Locate every Plasmodium malariae-infected red blood cell.
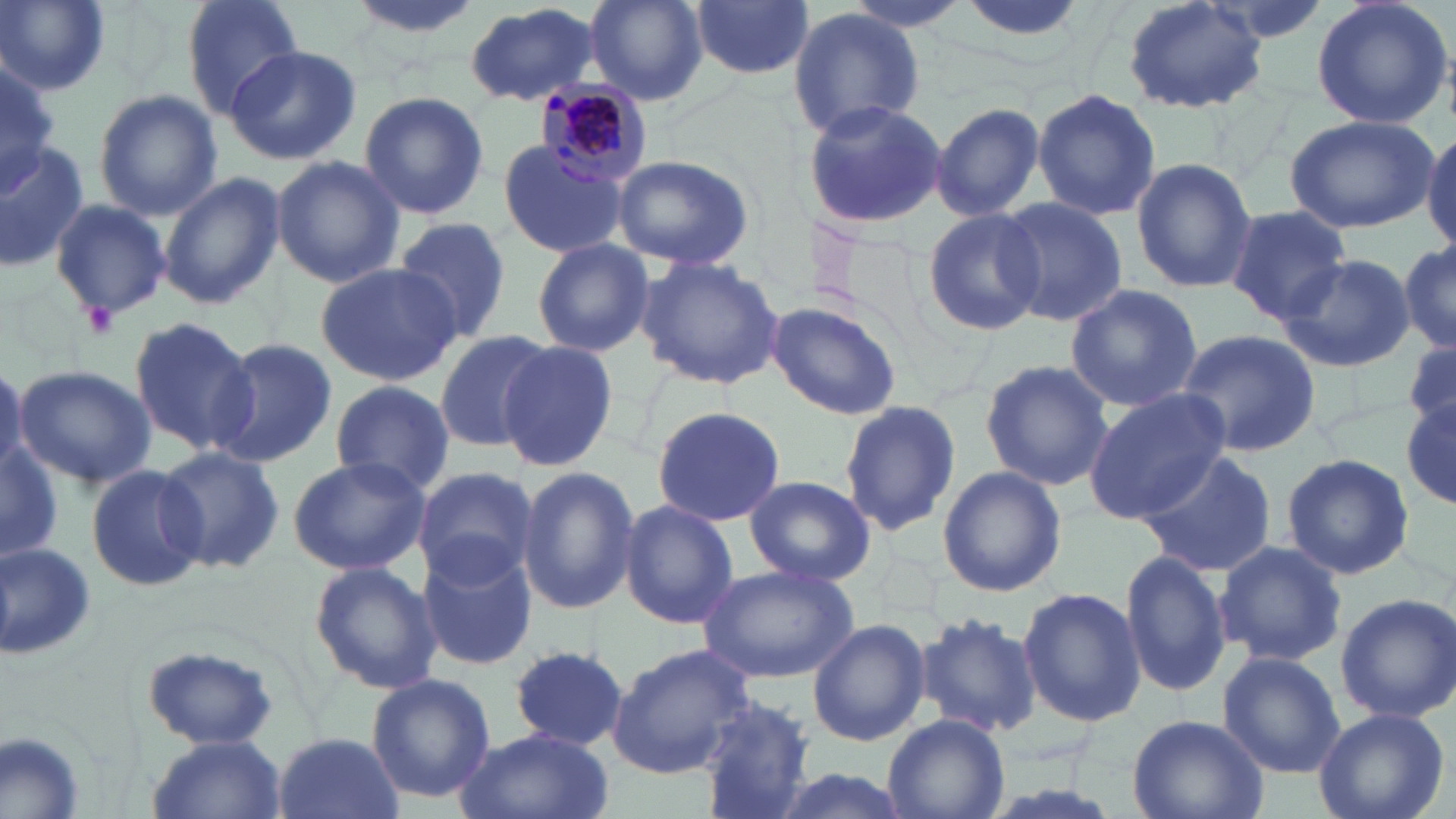
Approximate bounding boxes as (x1, y1, x2, y2) in pixels.
Plasmodium malariae-infected red blood cells: (534, 76, 654, 186).

slide_level_diagnosis: Plasmodium malariae
modality: optical microscopy
image_size: 1456×819 pixels
stain: May-Grünwald-Giemsa
platelet_locations: 'approximate bounding boxes as (x1, y1, x2, y2) in pixels: (82, 302, 118, 336)'
preparation: thin blood film
field_of_view: one of a larger specimen
magnification: 1000x
uninfected_red_blood_cell_locations: 'approximate bounding boxes as (x1, y1, x2, y2) in pixels: (1, 0, 112, 94), (180, 0, 304, 120), (345, 0, 485, 44), (586, 0, 708, 104), (837, 0, 975, 33), (952, 0, 1096, 49), (1120, 0, 1270, 113), (1310, 0, 1455, 131), (692, 1, 813, 80), (464, 4, 603, 106), (789, 7, 925, 138), (224, 45, 362, 165), (1, 55, 58, 193), (93, 88, 222, 220), (1031, 88, 1161, 221), (359, 90, 489, 220), (804, 100, 948, 230), (930, 102, 1047, 221), (1284, 115, 1438, 233), (1424, 126, 1456, 256), (0, 139, 89, 273), (496, 139, 628, 259), (611, 154, 756, 272), (269, 156, 405, 286), (1130, 158, 1257, 292), (159, 171, 285, 308), (49, 196, 172, 320), (993, 197, 1129, 325), (1221, 205, 1353, 322), (921, 207, 1046, 335), (392, 217, 513, 344), (1398, 236, 1455, 354), (531, 239, 656, 357), (1278, 253, 1416, 373), (636, 256, 785, 391), (314, 263, 462, 386), (1064, 284, 1204, 412), (768, 302, 902, 421), (127, 316, 260, 457), (433, 329, 556, 452), (1173, 330, 1320, 459), (1404, 335, 1456, 436), (211, 338, 336, 468), (497, 340, 619, 470), (980, 358, 1111, 490), (0, 361, 27, 482), (13, 365, 155, 489), (330, 379, 454, 497), (1084, 387, 1233, 523), (837, 397, 961, 538), (1402, 398, 1456, 511), (651, 405, 786, 527), (1, 437, 62, 564), (155, 444, 286, 574), (1135, 451, 1278, 577), (1279, 453, 1415, 580), (285, 455, 430, 575), (83, 462, 207, 593), (516, 464, 639, 616), (938, 465, 1066, 597), (412, 467, 540, 589), (744, 476, 876, 585), (619, 500, 738, 630), (0, 541, 96, 661), (1213, 541, 1349, 667), (416, 542, 538, 671), (1119, 548, 1234, 697), (309, 561, 442, 694), (696, 563, 860, 683), (1017, 586, 1145, 727), (1335, 592, 1456, 722), (913, 612, 1042, 736), (808, 620, 929, 746), (608, 641, 758, 780), (136, 643, 286, 750), (509, 646, 628, 751), (1217, 650, 1347, 777), (367, 672, 495, 804), (695, 697, 815, 819), (1312, 705, 1450, 819), (1126, 713, 1270, 819), (883, 715, 1008, 819), (453, 728, 613, 819), (1, 730, 88, 819), (274, 731, 402, 819), (144, 734, 287, 818)'